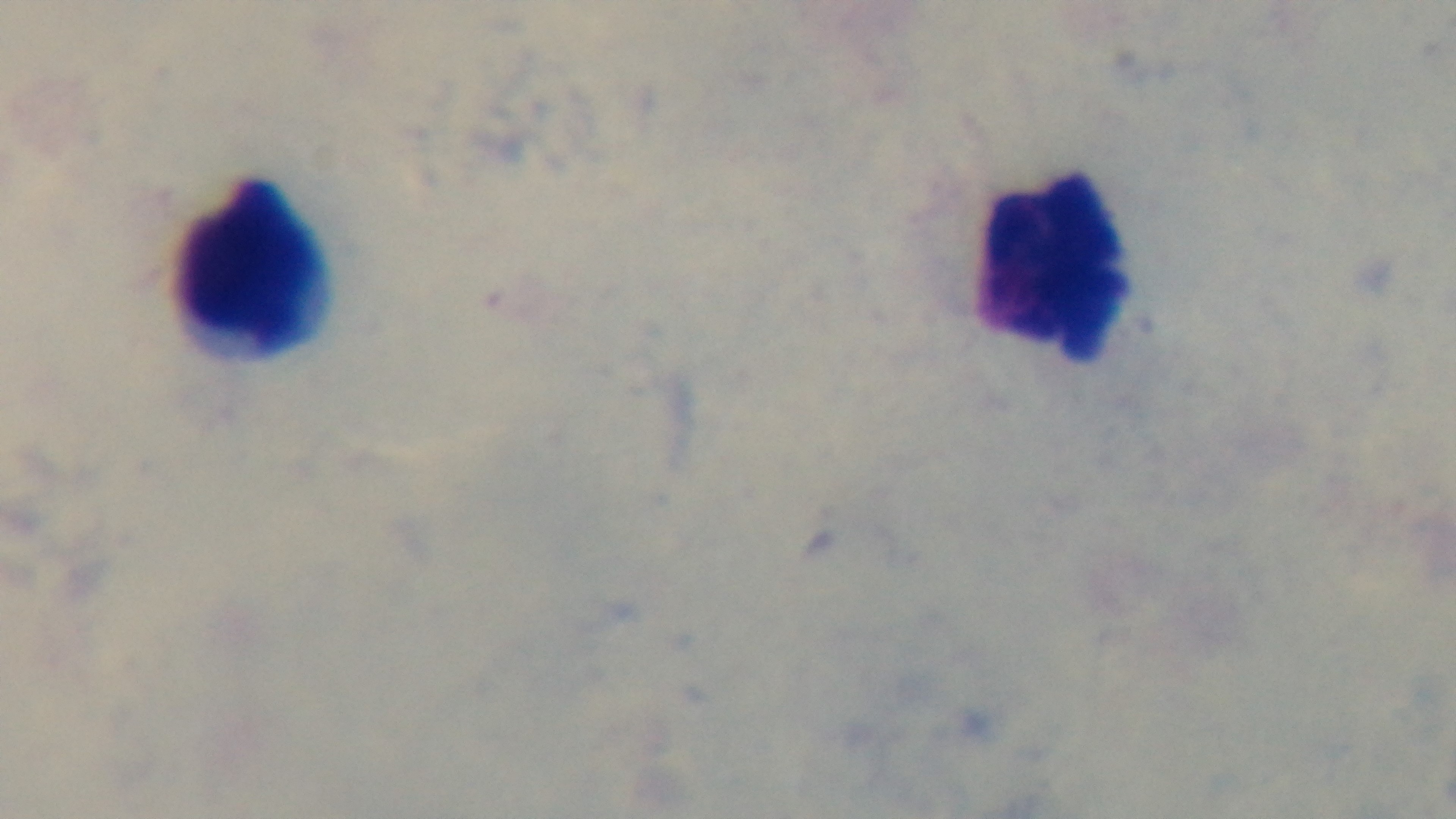

Summary:
  - Preparation: thick
  - Modality: light microscopy
  - Malaria status: negative
  - Field of view: single
  - Objective: 100x oil immersion
  - Capture: mounted 4K digital camera
  - Stain: Giemsa